Assess this cell for malaria.
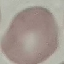

It is uninfected.

Summary:
  - Image type: automatically extracted cell patch, resized to 64 × 64 pixels
  - Capture: smartphone camera at the microscope eyepiece
  - Stain: Giemsa
  - Preparation: thin smear